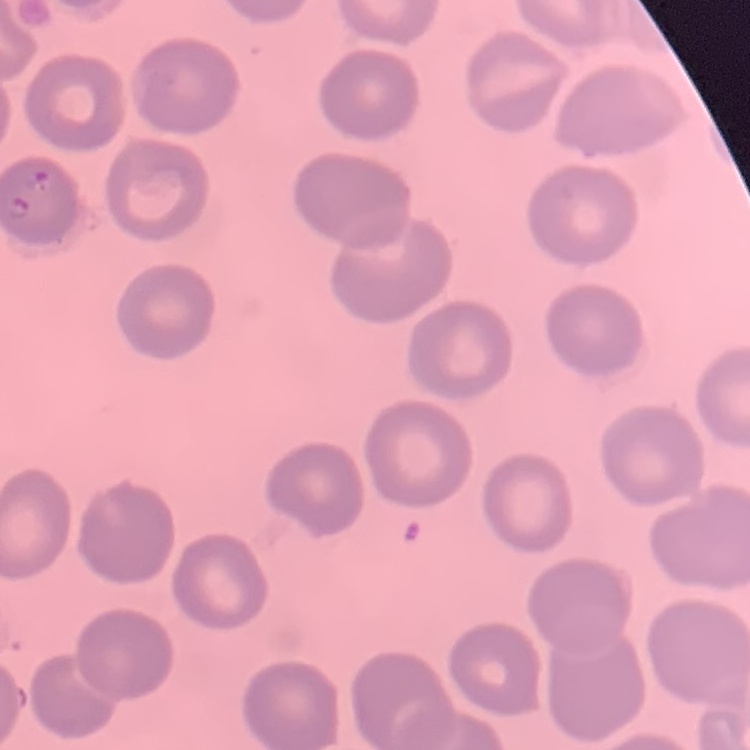
red blood cell morphology = no rouleaux formation
preparation = thin blood film
stain = Field's or Giemsa
image type = one tile cut from a larger photomicrograph